Point out each Plasmodium parasite.
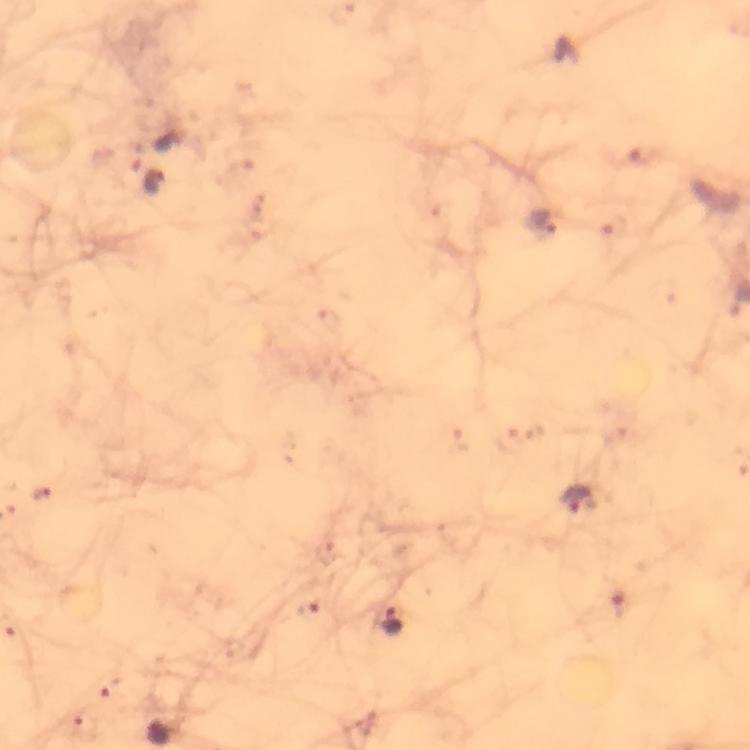

Approximate centers as (x, y) in pixels.
Plasmodium parasites: (155, 183), (539, 222), (576, 500), (391, 621).

Summary:
  - Capture: smartphone camera through the microscope
  - Preparation: thick smear
  - Magnification: 100x
  - Immersion oil: applied
  - Image size: 750×750 pixels
  - Cropped from: one field of view
  - Context: from a diagnostic examination for malaria
  - Stain: Giemsa